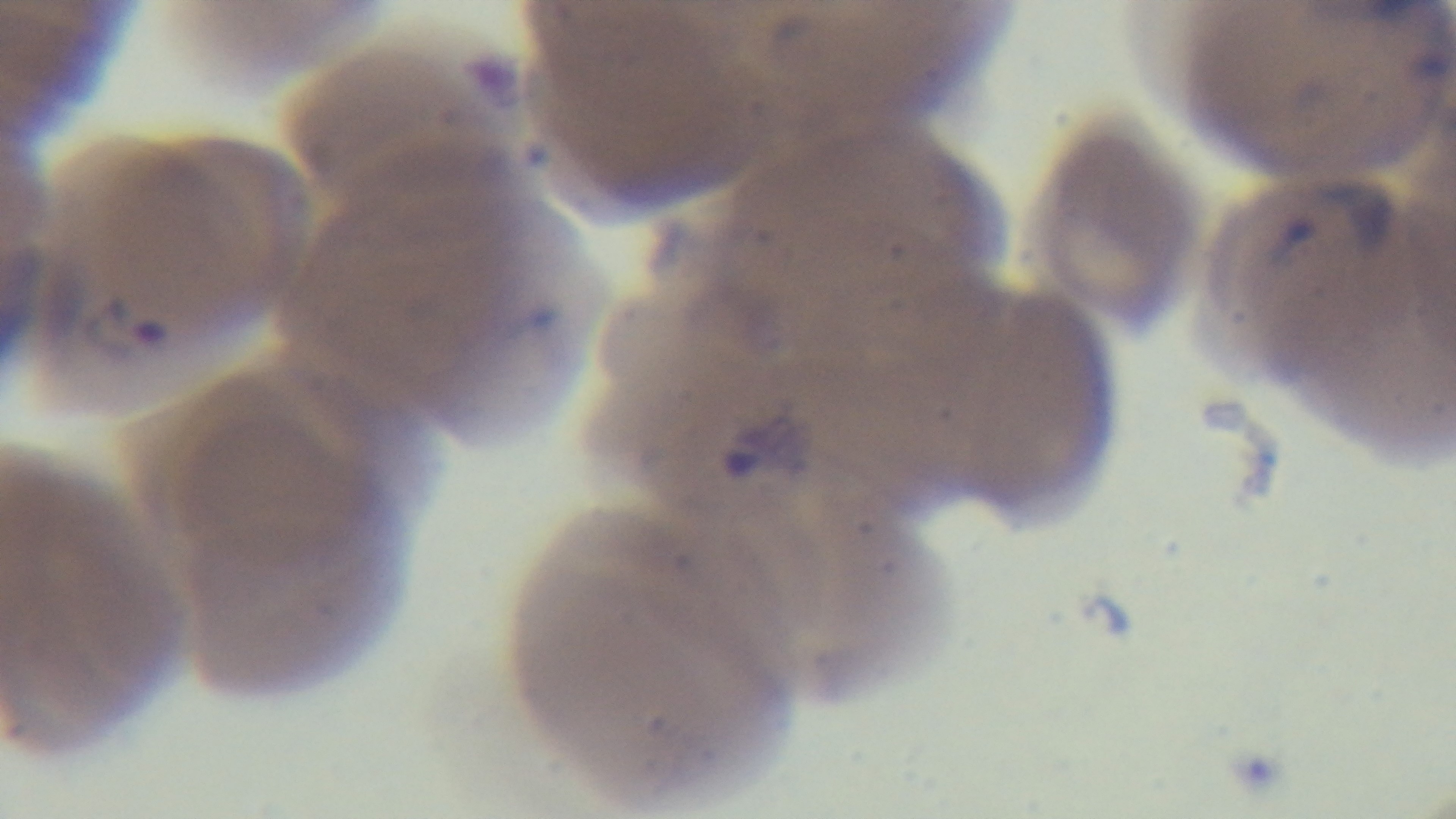
Summary:
  - Field of view: one from the slide
  - Malaria status: positive
  - Stain: Giemsa
  - Capture: mounted 4K digital camera
  - Objective: 100x oil immersion
  - Preparation: thin
  - Modality: light microscopy